Classify this cell by malaria status.
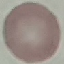

Uninfected.

Giemsa-stained preparation. Photographed with a smartphone camera at the microscope eyepiece. Automatically extracted cell patch, resized to 64 × 64 pixels. Thin smear of blood.